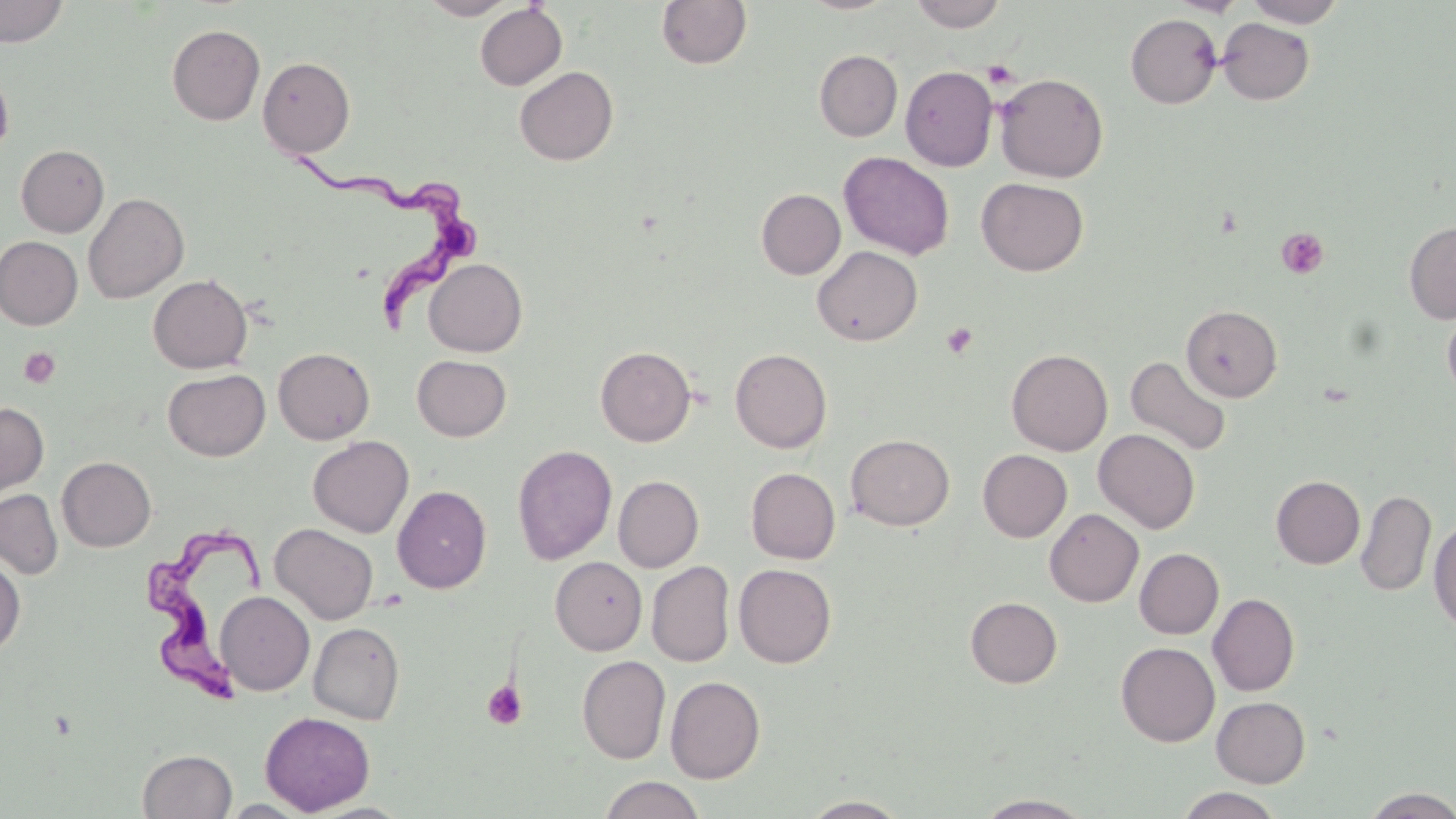
Summary:
  - Coordinate format: approximate bounding boxes as (x1, y1, x2, y2) in pixels
  - Uninfected red blood cell locations: (0, 0, 69, 47), (420, 0, 516, 19), (656, 0, 752, 69), (799, 0, 900, 15), (909, 0, 1006, 32), (1169, 0, 1247, 16), (1244, 0, 1346, 27), (474, 3, 567, 90), (1125, 13, 1222, 108), (1217, 17, 1314, 104), (167, 24, 265, 125), (814, 50, 903, 142), (257, 56, 355, 158), (514, 66, 618, 166), (900, 66, 998, 171), (0, 68, 14, 160), (994, 72, 1109, 183), (16, 144, 109, 237), (839, 151, 955, 260), (976, 177, 1089, 276), (756, 189, 845, 279), (83, 192, 189, 304), (1404, 221, 1456, 324), (0, 237, 83, 329), (812, 245, 923, 346), (424, 258, 527, 356), (148, 274, 252, 373), (1441, 304, 1456, 404), (1181, 305, 1282, 402), (595, 345, 696, 447), (273, 347, 374, 444), (730, 348, 832, 453), (739, 349, 835, 565), (1007, 349, 1113, 456), (412, 355, 511, 441), (1125, 355, 1233, 458), (163, 368, 270, 461), (0, 402, 48, 498), (1093, 428, 1200, 533), (846, 434, 955, 530), (307, 435, 414, 538), (512, 444, 617, 565), (978, 449, 1071, 542), (57, 456, 155, 552), (746, 468, 840, 564), (613, 475, 704, 572), (1271, 475, 1365, 569), (392, 485, 491, 594), (0, 489, 63, 579), (1356, 489, 1435, 597), (1044, 508, 1143, 606), (1429, 517, 1456, 634), (270, 523, 378, 625), (1135, 548, 1224, 639), (0, 555, 26, 657), (551, 556, 647, 655), (646, 561, 735, 667), (733, 563, 837, 668), (216, 591, 314, 695), (1208, 593, 1300, 696), (965, 597, 1062, 687), (308, 622, 405, 724), (1116, 642, 1220, 747), (577, 654, 671, 764), (665, 675, 765, 783), (1211, 696, 1310, 787), (260, 711, 375, 815), (138, 748, 237, 819), (598, 776, 706, 819), (1360, 787, 1456, 818), (1175, 788, 1285, 819), (973, 794, 1095, 818), (800, 795, 910, 818), (220, 799, 314, 817), (306, 802, 414, 819)
  - Platelet locations: (983, 61, 1019, 88), (1276, 227, 1328, 279), (941, 322, 978, 360), (19, 347, 60, 389), (482, 680, 527, 730)
  - Trypanosoma brucei locations: (298, 156, 485, 332), (145, 519, 267, 702)
  - Slide-level diagnosis: Trypanosoma brucei
  - Preparation: thin blood film
  - Magnification: 1000x
  - Modality: optical microscopy
  - Image size: 1456×819 pixels
  - Field of view: single
  - Stain: May-Grünwald-Giemsa